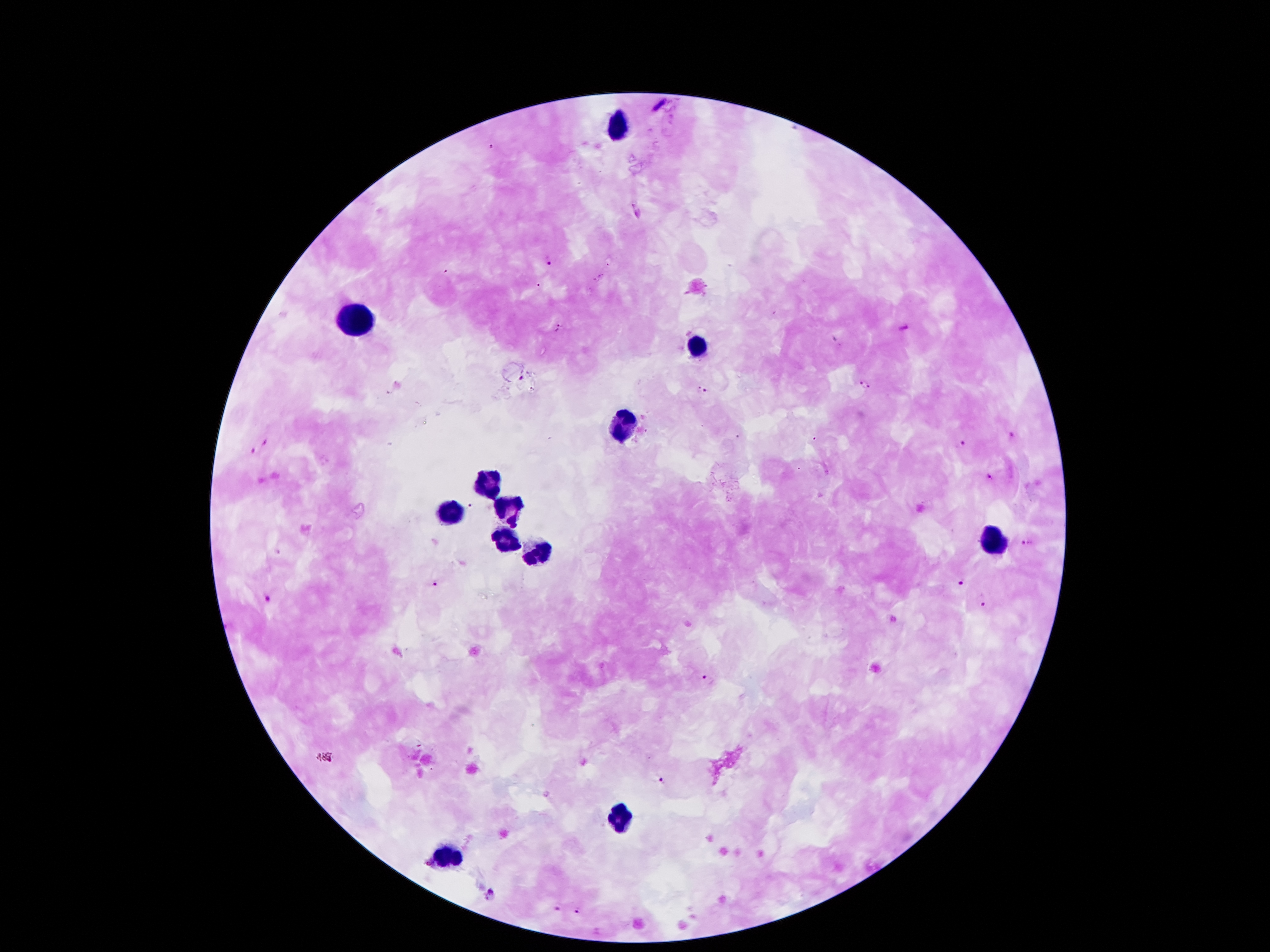

Approximate centers as (x, y) in pixels.
Summary:
  - Leukocyte locations: (618, 123), (356, 320), (696, 344), (624, 428), (490, 485), (450, 511), (510, 514), (505, 542), (994, 542), (540, 554), (620, 816), (447, 857)
  - Plasmodium parasite locations: (491, 145), (548, 259), (558, 328), (903, 328), (522, 378), (863, 385), (704, 390), (1011, 436), (264, 439), (962, 444), (254, 452), (989, 476), (470, 504), (1025, 542), (961, 579), (438, 584), (269, 597), (985, 605), (708, 682), (661, 779), (489, 895), (555, 908), (579, 912)
  - Stain: Giemsa
  - Preparation: thick blood smear
  - Patient malaria status: infected with Plasmodium falciparum
  - Magnification: 100x
  - Image size: 1270×952 pixels
  - Field of view: single
  - Capture: smartphone through the microscope eyepiece